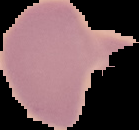

Summary:
  - Preparation: thin blood smear
  - Image size: 139×130 pixels
  - Result: no Plasmodium parasites seen
  - Image type: cell region segmented out of the field of view; surrounding area masked to black